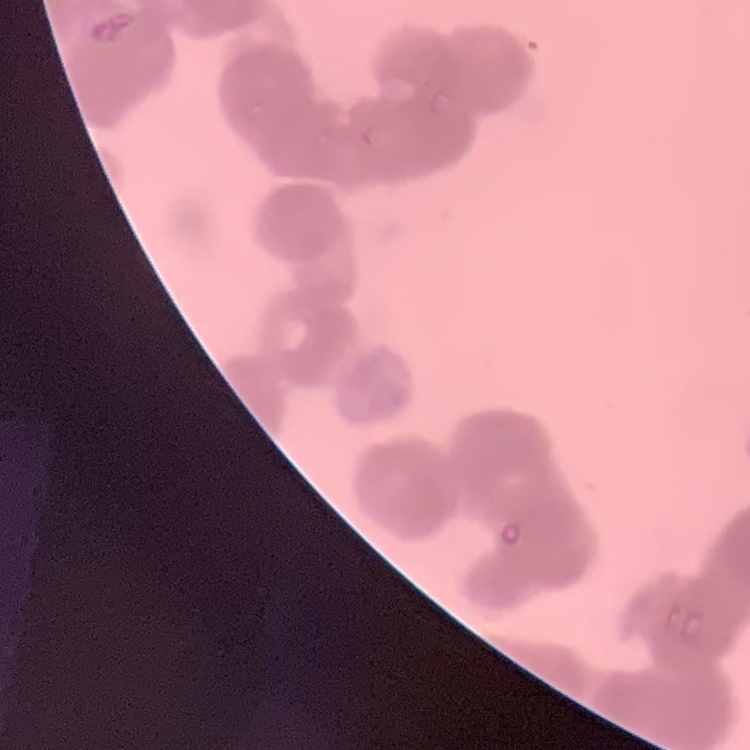 The red blood cells show rouleaux formation. Square crop of a larger photomicrograph. Thin blood smear. Stained with either Field's or Giemsa.